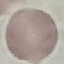
Result: negative for malaria parasites. Thin blood smear. Cell patch, automatically extracted from a larger field of view and resized to 64 × 64 pixels. Giemsa-stained preparation. Photographed with a smartphone camera at the microscope eyepiece.